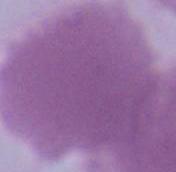
Summary:
  - Modality: micrograph
  - Identification: red blood cell
  - Magnification: 1000x